Outline each Plasmodium ovale-infected red blood cell.
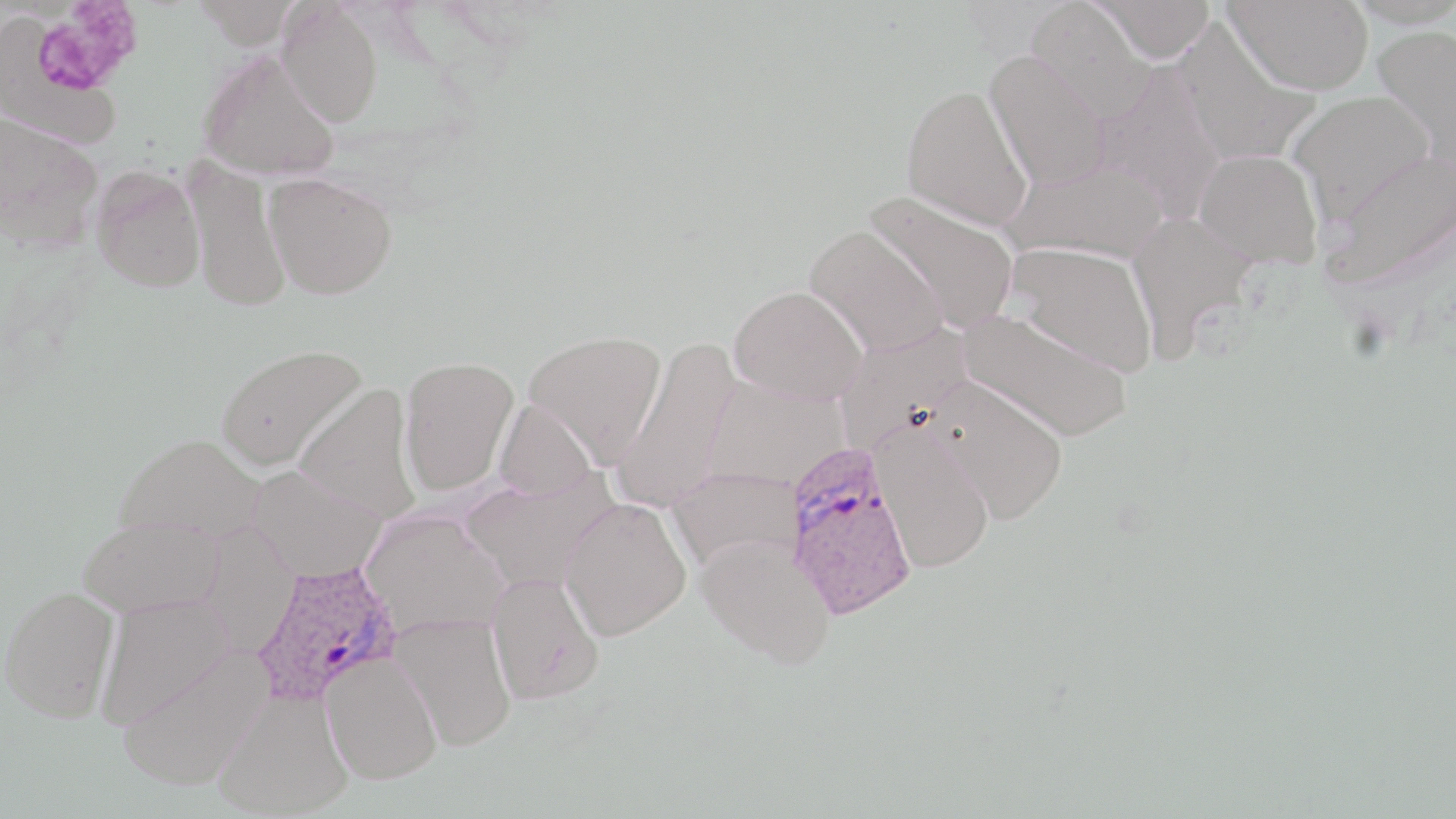

Approximate bounding boxes as named x1/y1/x2/y2 corners in pixels.
Plasmodium ovale-infected red blood cells: (x1=783, y1=445, x2=918, y2=621), (x1=253, y1=562, x2=402, y2=706).

Summary:
  - Uninfected red blood cell locations: (x1=191, y1=0, x2=302, y2=49), (x1=1225, y1=0, x2=1372, y2=96), (x1=1027, y1=1, x2=1154, y2=125), (x1=1092, y1=1, x2=1214, y2=64), (x1=277, y1=3, x2=384, y2=127), (x1=1, y1=13, x2=123, y2=149), (x1=1174, y1=20, x2=1320, y2=167), (x1=1373, y1=24, x2=1456, y2=173), (x1=197, y1=49, x2=340, y2=182), (x1=985, y1=52, x2=1111, y2=192), (x1=1095, y1=62, x2=1228, y2=223), (x1=901, y1=84, x2=1033, y2=231), (x1=1287, y1=91, x2=1436, y2=223), (x1=0, y1=111, x2=103, y2=251), (x1=1194, y1=148, x2=1323, y2=269), (x1=1322, y1=149, x2=1456, y2=289), (x1=1001, y1=156, x2=1168, y2=265), (x1=181, y1=159, x2=293, y2=313), (x1=90, y1=166, x2=205, y2=293), (x1=263, y1=172, x2=398, y2=300), (x1=864, y1=191, x2=1019, y2=335), (x1=1126, y1=210, x2=1258, y2=359), (x1=805, y1=225, x2=947, y2=357), (x1=1007, y1=242, x2=1158, y2=378), (x1=728, y1=284, x2=867, y2=406), (x1=958, y1=308, x2=1133, y2=443), (x1=834, y1=325, x2=972, y2=453), (x1=523, y1=330, x2=667, y2=466), (x1=611, y1=336, x2=742, y2=512), (x1=216, y1=343, x2=367, y2=471), (x1=399, y1=356, x2=519, y2=496), (x1=702, y1=377, x2=847, y2=491), (x1=927, y1=378, x2=1069, y2=524), (x1=295, y1=384, x2=421, y2=523), (x1=494, y1=399, x2=597, y2=501), (x1=872, y1=425, x2=995, y2=573), (x1=114, y1=433, x2=267, y2=545), (x1=246, y1=464, x2=387, y2=582), (x1=666, y1=468, x2=801, y2=573), (x1=459, y1=472, x2=620, y2=594), (x1=560, y1=497, x2=691, y2=640), (x1=360, y1=509, x2=510, y2=640), (x1=78, y1=516, x2=223, y2=618), (x1=199, y1=521, x2=300, y2=657), (x1=697, y1=534, x2=836, y2=669), (x1=487, y1=572, x2=605, y2=706), (x1=1, y1=584, x2=120, y2=722), (x1=95, y1=595, x2=233, y2=727), (x1=391, y1=613, x2=517, y2=751), (x1=116, y1=646, x2=272, y2=792), (x1=321, y1=652, x2=442, y2=784), (x1=214, y1=688, x2=352, y2=818)
  - Platelet locations: (x1=28, y1=6, x2=140, y2=105)
  - Slide-level diagnosis: Plasmodium ovale
  - Magnification: 1000x
  - Preparation: thin blood film
  - Stain: May-Grünwald-Giemsa
  - Field of view: single
  - Modality: optical microscopy
  - Image size: 1456×819 pixels